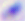
identification = Toxoplasma gondii
modality = photomicrograph
magnification = 400x